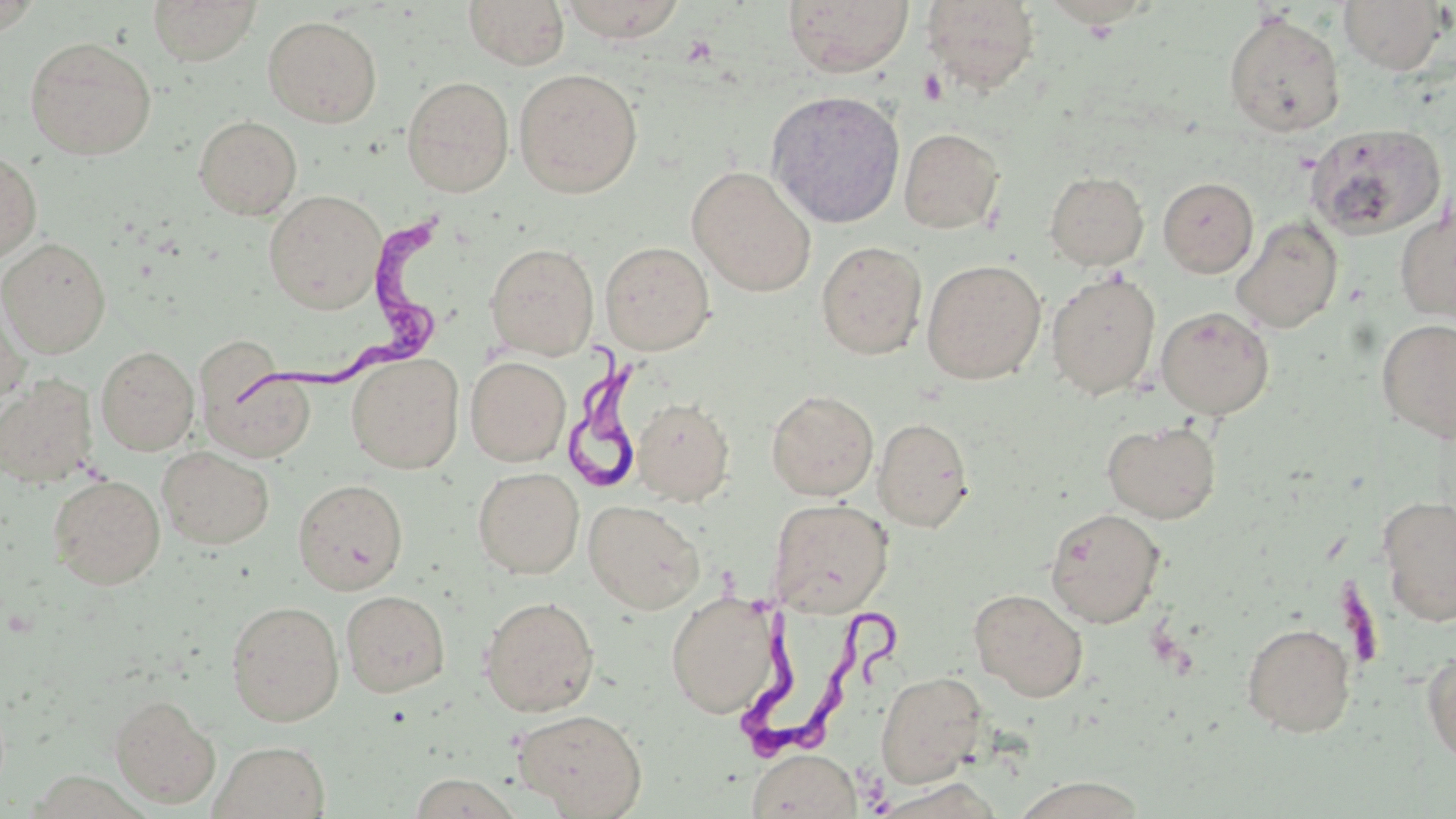

slide-level diagnosis = Trypanosoma brucei
magnification = 1000x
field of view = one of a larger specimen
preparation = thin blood smear
modality = optical microscopy
platelet locations = approximate bounding boxes as (x1, y1, x2, y2) in pixels: (918, 68, 947, 105)
stain = May-Grünwald-Giemsa
image size = 1456×819 pixels
uninfected red blood cell locations = approximate bounding boxes as (x1, y1, x2, y2) in pixels: (147, 0, 262, 65), (463, 0, 570, 70), (557, 0, 688, 42), (782, 0, 914, 77), (920, 0, 1039, 95), (1338, 0, 1451, 74), (1223, 12, 1346, 138), (263, 16, 383, 127), (24, 36, 157, 160), (514, 68, 643, 197), (402, 76, 514, 197), (766, 89, 906, 229), (194, 115, 302, 219), (1306, 123, 1446, 241), (899, 127, 1005, 234), (0, 150, 42, 264), (687, 166, 817, 296), (1045, 171, 1149, 270), (1158, 177, 1258, 277), (264, 189, 386, 313), (1394, 197, 1456, 325), (1231, 216, 1343, 333), (0, 237, 111, 357), (600, 240, 715, 354), (816, 240, 927, 359), (485, 242, 599, 359), (922, 259, 1046, 384), (1046, 270, 1161, 400), (0, 285, 31, 410), (1156, 306, 1274, 419), (1376, 318, 1456, 443), (96, 346, 199, 454), (347, 353, 464, 473), (466, 356, 570, 466), (200, 362, 316, 464), (0, 375, 99, 488), (766, 389, 879, 501), (633, 397, 734, 505), (874, 417, 973, 532), (1102, 419, 1221, 523), (157, 446, 274, 549), (473, 467, 584, 579), (47, 474, 165, 589), (293, 478, 408, 595), (1377, 495, 1456, 625), (769, 498, 894, 617), (584, 500, 704, 614), (1044, 507, 1167, 628), (969, 588, 1088, 702), (340, 590, 450, 696), (666, 591, 782, 718), (479, 595, 600, 717), (226, 600, 344, 725), (1242, 622, 1356, 738), (1422, 647, 1456, 770), (874, 671, 987, 788), (109, 694, 221, 808), (513, 708, 648, 817), (210, 741, 330, 819), (748, 748, 861, 819), (1008, 775, 1150, 819), (873, 779, 1004, 819)
Trypanosoma brucei locations = approximate bounding boxes as (x1, y1, x2, y2) in pixels: (241, 207, 446, 416), (565, 346, 654, 486), (711, 593, 914, 770)